Report the malaria status of this cell.
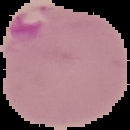
It is parasitized.

preparation: thin blood smear
image_type: segmented cell region on a black background
image_size: 130×130 pixels